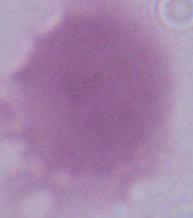

identification = erythrocyte
magnification = 1000x
modality = photomicrograph